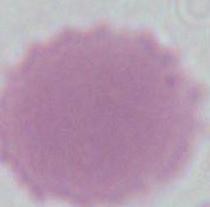
magnification = 1000x
modality = micrograph
identification = red blood cell